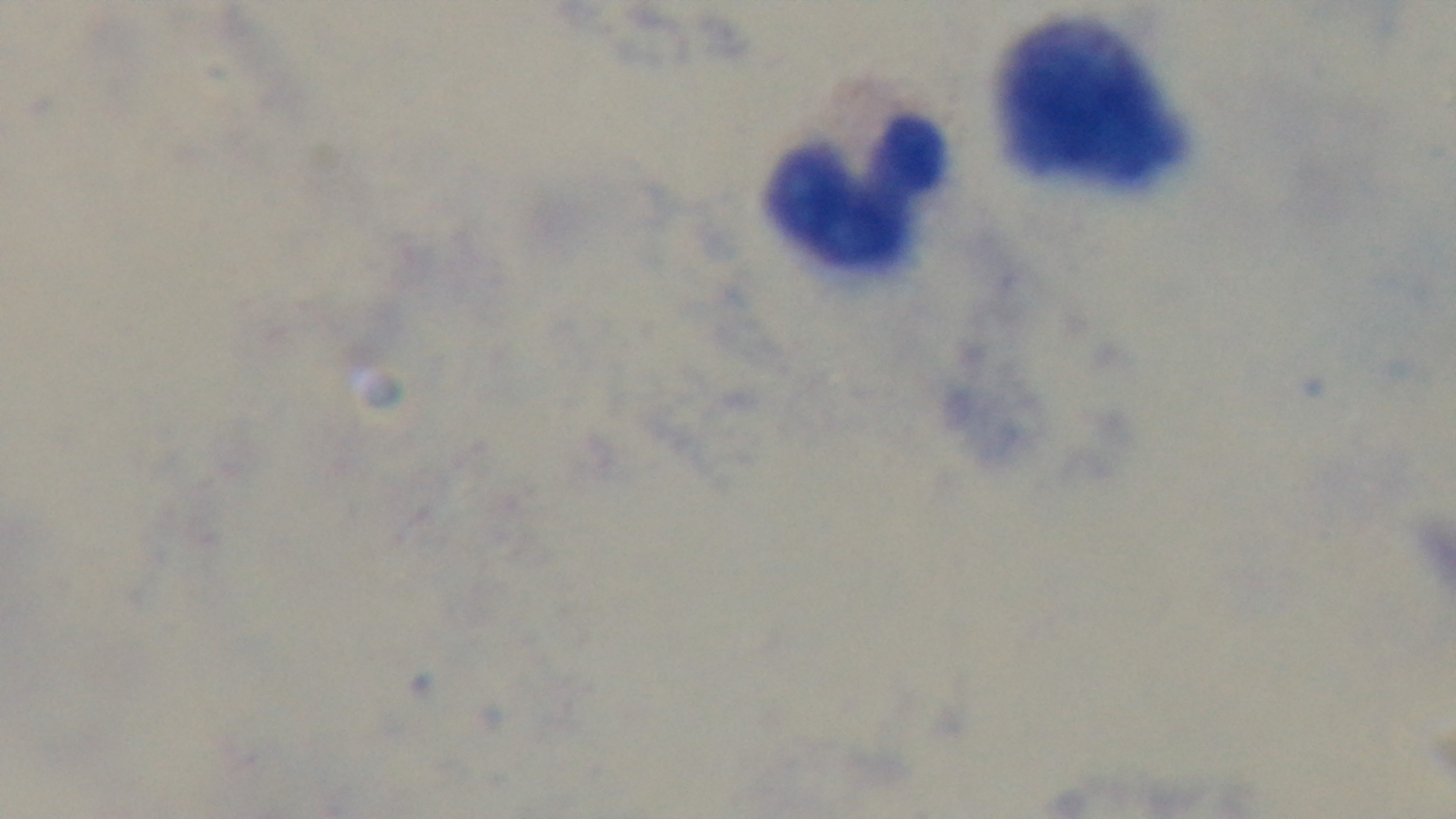
Preparation: thick smear. Malaria status: uninfected. Oil-immersion objective, 100x. Giemsa stain. Captured with a mounted 4K digital camera. Light microscopy. Single field of view.